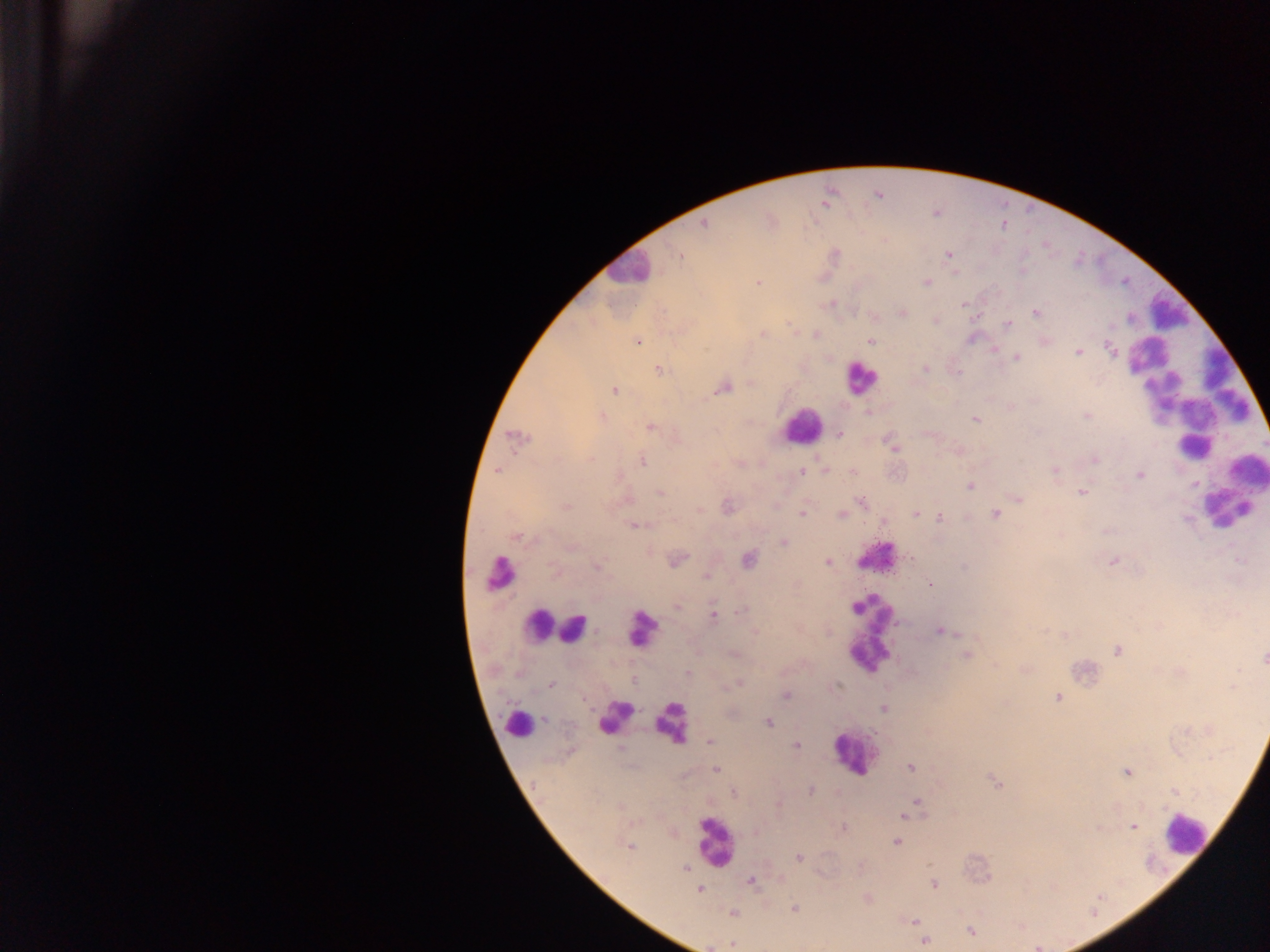

capture = mobile-phone photograph through a microscope
leukocyte locations = approximate centers as {x, y} in pixels: {620, 270}, {1185, 400}, {801, 425}, {1227, 498}, {562, 630}, {869, 635}, {673, 727}, {854, 763}, {709, 835}, {1181, 846}
field of view = single
Plasmodium parasite locations = approximate centers as {x, y} in pixels: {703, 225}, {882, 241}, {679, 251}, {836, 253}, {948, 255}, {925, 281}, {756, 282}, {901, 312}, {1037, 315}, {933, 320}, {788, 321}, {1006, 323}, {761, 334}, {870, 340}, {638, 342}, {1108, 346}, {994, 349}, {1077, 353}, {1017, 356}, {925, 369}, {658, 371}, {1147, 382}, {750, 384}, {727, 387}, {615, 389}, {605, 416}, {1087, 416}, {975, 419}, {647, 425}, {840, 433}, {894, 450}, {642, 459}, {1095, 459}, {739, 462}, {825, 470}, {801, 471}, {1055, 472}, {1139, 475}, {1194, 486}, {971, 488}, {1082, 493}, {661, 494}, {1019, 498}, {862, 502}, {565, 506}, {700, 510}, {915, 513}, {801, 514}, {840, 514}, {921, 514}, {994, 514}, {941, 516}, {884, 522}, {634, 526}, {516, 537}, {782, 543}, {676, 558}, {747, 560}, {1113, 561}, {829, 562}, {597, 566}, {554, 571}, {706, 577}, {930, 583}, {677, 606}, {743, 609}, {714, 614}, {1044, 630}, {755, 631}, {940, 632}, {957, 634}, {1065, 635}, {1116, 650}, {966, 655}, {1263, 659}, {686, 671}, {632, 679}, {739, 684}, {552, 686}, {839, 686}, {1234, 686}, {785, 694}, {1057, 698}, {883, 709}, {543, 718}, {769, 723}, {710, 742}, {797, 746}, {620, 747}, {910, 767}, {717, 770}, {1126, 772}, {991, 779}, {997, 784}, {734, 792}, {917, 799}, {777, 804}, {901, 816}, {1134, 826}, {844, 828}, {896, 843}, {629, 845}, {799, 857}, {928, 864}, {686, 868}, {751, 882}, {933, 884}, {1054, 886}, {700, 890}, {868, 899}, {795, 909}, {733, 914}, {1092, 916}, {912, 921}, {971, 931}, {925, 941}, {732, 944}
image size = 1270×952 pixels
preparation = thick blood film
country = Ghana